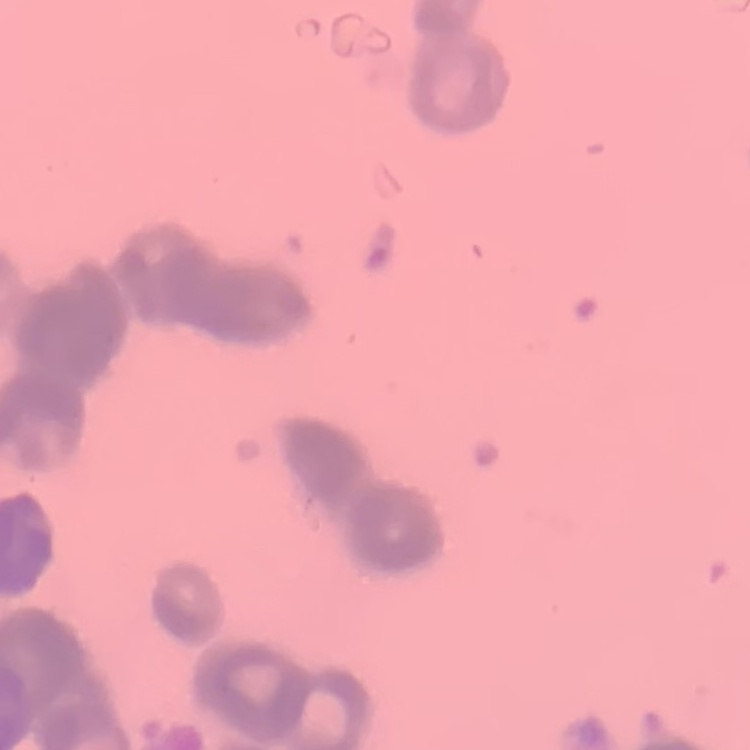

Summary:
  - Erythrocyte morphology: rouleaux formation
  - Stain: Field's or Giemsa
  - Image type: square crop of a larger photomicrograph
  - Preparation: thin peripheral smear